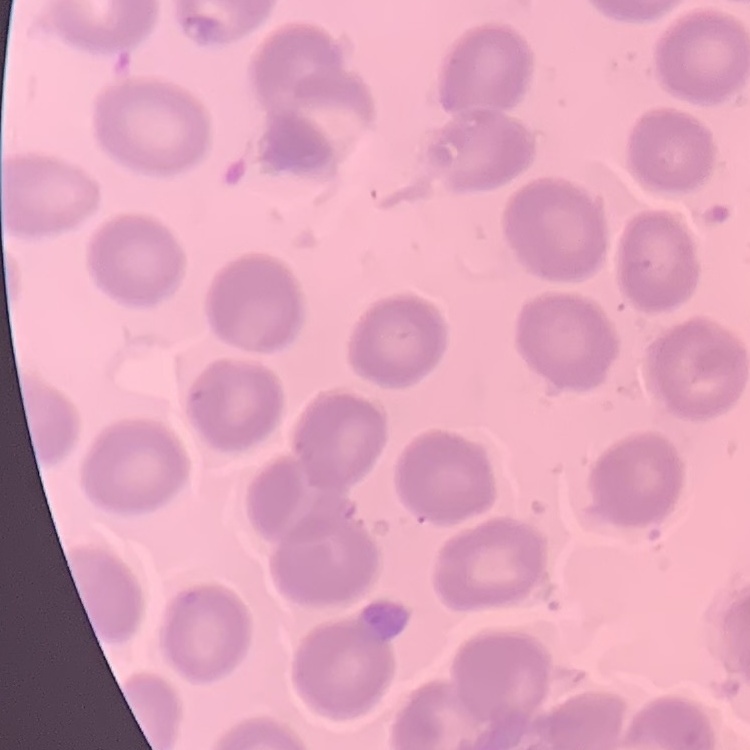

Summary:
  - Erythrocyte morphology: no rouleaux formation
  - Stain: Field's or Giemsa
  - Image type: one tile cut from a larger photomicrograph
  - Preparation: thin blood smear